Outline platelets.
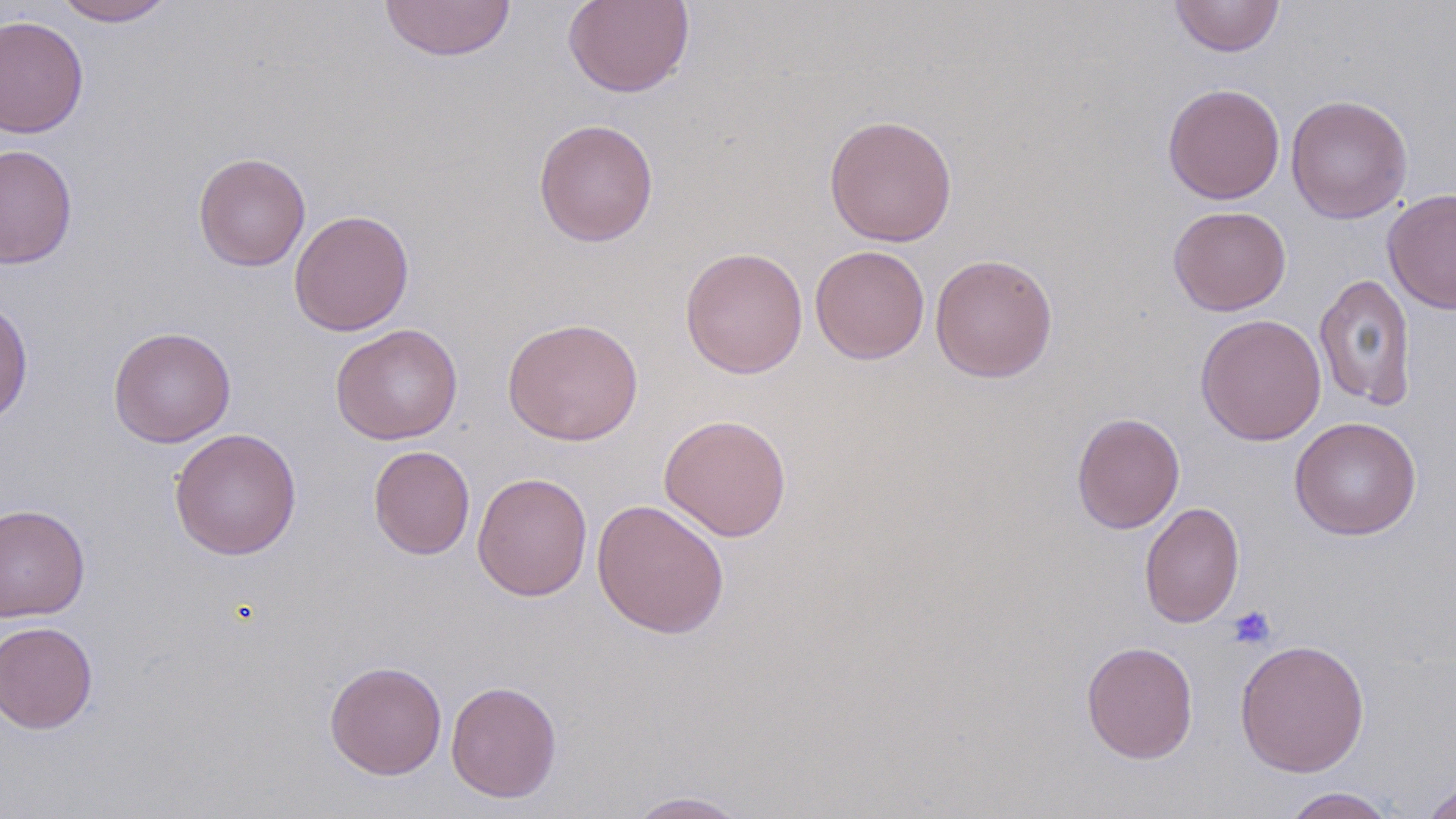

Approximate bounding boxes as (x1,y1)-(x2,y2) corner pairs in pixels.
Platelets: (1227,605)-(1276,650).

Uninfected red blood cell locations: (52,0)-(177,26), (379,0)-(517,62), (562,0)-(696,98), (1170,0)-(1285,57), (0,14)-(89,139), (1162,83)-(1286,204), (1286,94)-(1413,223), (823,113)-(958,247), (533,118)-(659,247), (0,144)-(78,269), (193,152)-(310,271), (1383,188)-(1456,314), (1168,205)-(1292,316), (289,209)-(415,336), (809,245)-(929,364), (680,246)-(808,379), (930,252)-(1058,383), (1314,272)-(1417,411), (0,298)-(33,427), (1195,313)-(1327,446), (502,318)-(644,445), (330,323)-(464,444), (108,326)-(236,447), (1071,412)-(1185,533), (659,413)-(792,542), (1289,416)-(1422,540), (169,428)-(302,560), (368,445)-(475,559), (472,472)-(593,601), (591,498)-(729,639), (1139,502)-(1244,628), (0,503)-(91,622), (0,621)-(98,734), (1234,638)-(1370,777), (1080,640)-(1199,764), (324,660)-(447,779), (445,680)-(562,803), (1421,777)-(1456,819), (1279,787)-(1400,818), (625,790)-(754,818). Slide-level diagnosis: negative for blood parasites. 1000x magnification. May-Grünwald-Giemsa-stained preparation. Thin blood smear. Light microscopy. One field of a larger specimen. Image is 1456×819 pixels.